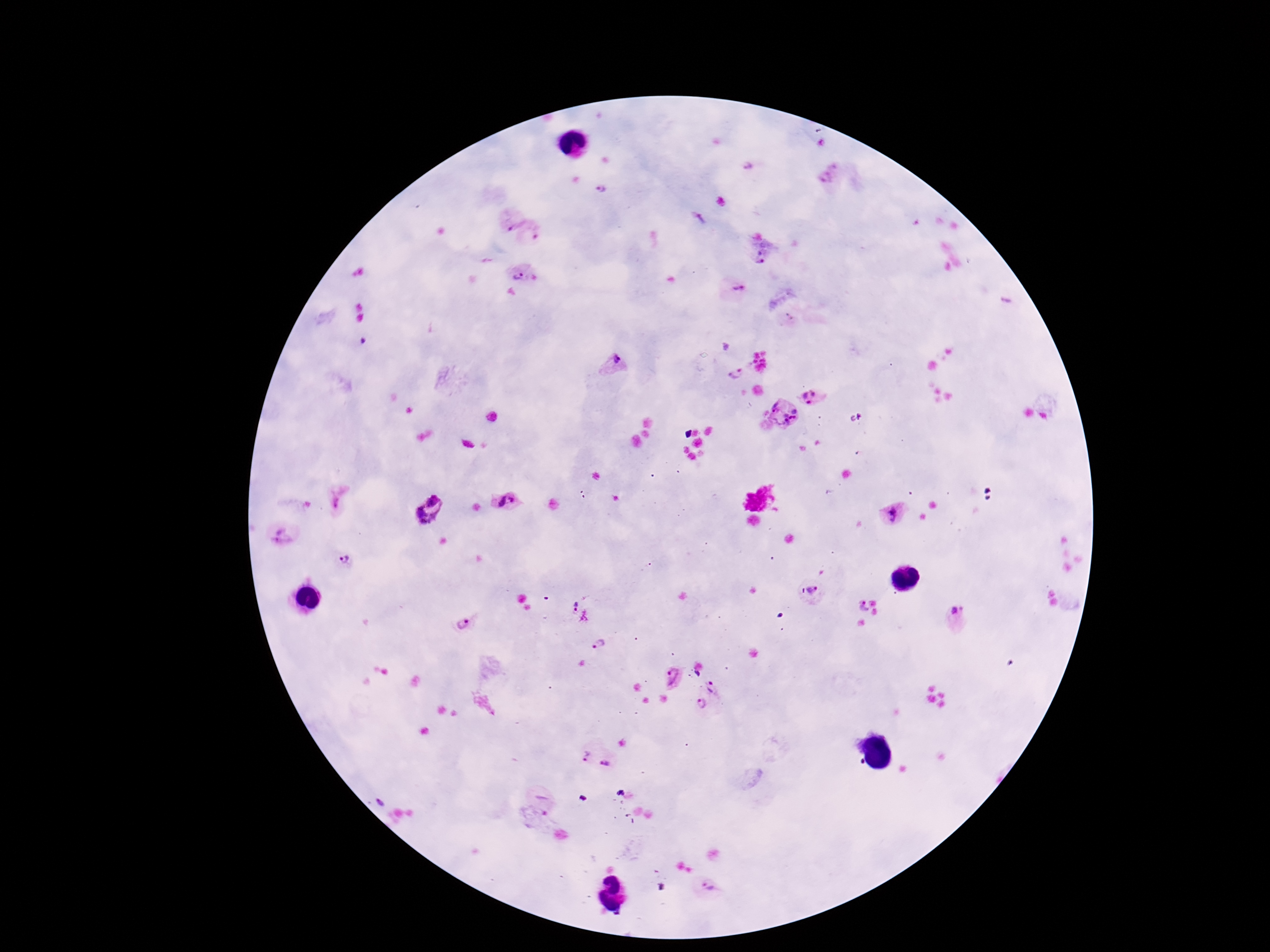
Approximate centers as (x, y) in pixels.
Summary:
  - Plasmodium parasite locations: (747, 165), (828, 173), (601, 188), (510, 218), (535, 235), (760, 261), (522, 275), (739, 287), (792, 315), (615, 362), (735, 373), (814, 397), (781, 411), (855, 417), (340, 501), (502, 501), (427, 511), (895, 513), (282, 538), (346, 561), (812, 591), (574, 602), (858, 604), (958, 615), (463, 624), (598, 642), (673, 681), (718, 686), (702, 706), (583, 754), (607, 762), (707, 885)
  - Capture: smartphone camera through the microscope eyepiece
  - Field of view: one from this slide
  - Preparation: thick blood smear
  - Image size: 1270×952 pixels
  - Magnification: 100x
  - Stain: Giemsa
  - Patient malaria status: infected